Identify the blood parasite species.
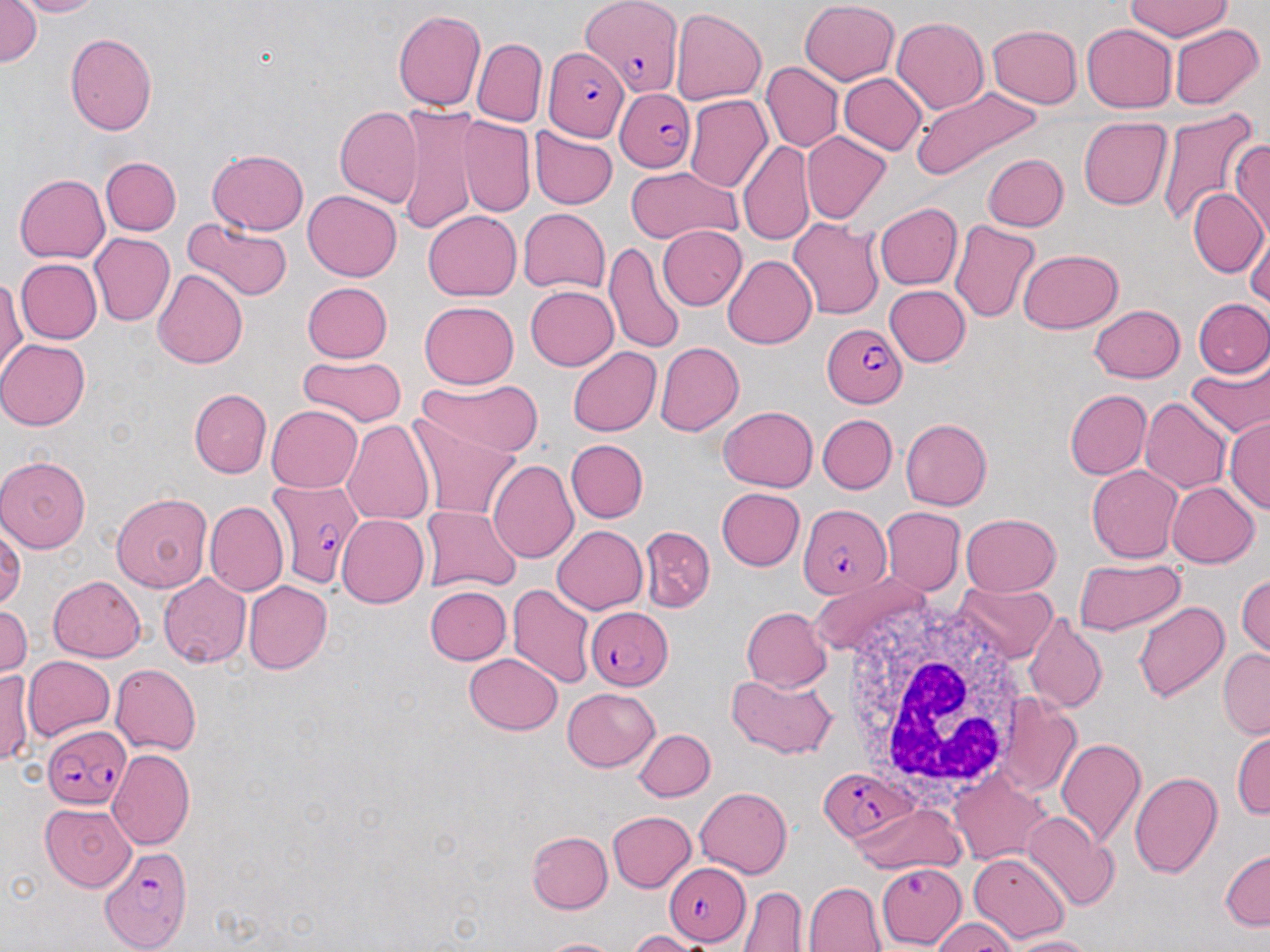

Plasmodium falciparum.

Approximate bounding boxes as (x1, y1, x2, y2) in pixels. Plasmodium falciparum-infected red blood cell locations: (580, 0, 684, 97), (542, 46, 630, 142), (613, 88, 693, 174), (822, 322, 907, 406), (267, 479, 363, 592), (798, 503, 890, 600), (584, 606, 672, 690), (42, 725, 132, 810), (818, 768, 915, 841), (100, 847, 192, 951), (876, 862, 968, 949), (663, 863, 750, 946). Uninfected red blood cell locations: (12, 0, 102, 17), (799, 0, 899, 84), (0, 1, 41, 67), (1123, 1, 1234, 41), (670, 8, 767, 106), (392, 10, 486, 110), (892, 16, 989, 116), (987, 23, 1082, 107), (1081, 23, 1177, 113), (1169, 24, 1264, 110), (65, 33, 158, 135), (472, 38, 546, 126), (761, 62, 843, 152), (839, 73, 927, 154), (820, 77, 914, 214), (910, 85, 1042, 183), (685, 95, 773, 193), (335, 107, 423, 207), (1156, 107, 1261, 232), (396, 108, 481, 234), (457, 116, 535, 217), (1078, 117, 1173, 210), (529, 126, 618, 209), (801, 132, 892, 225), (738, 141, 814, 246), (1229, 141, 1269, 243), (208, 148, 309, 235), (983, 154, 1068, 232), (100, 156, 181, 235), (626, 166, 742, 244), (14, 174, 109, 263), (1188, 188, 1267, 277), (304, 189, 401, 280), (874, 203, 963, 290), (518, 207, 610, 293), (423, 210, 522, 301), (787, 217, 885, 320), (182, 218, 294, 302), (1245, 218, 1270, 311), (948, 220, 1041, 325), (658, 224, 747, 309), (89, 232, 174, 326), (604, 243, 686, 356), (1018, 248, 1124, 333), (722, 255, 816, 349), (16, 258, 102, 343), (152, 269, 248, 370), (1, 277, 26, 381), (301, 282, 392, 362), (883, 284, 970, 366), (526, 285, 618, 371), (1194, 299, 1270, 377), (419, 301, 519, 388), (1089, 304, 1185, 383), (0, 339, 90, 430), (655, 341, 744, 436), (567, 346, 661, 437), (297, 354, 407, 427), (1186, 355, 1270, 440), (418, 377, 545, 458), (189, 388, 272, 478), (1073, 388, 1161, 557), (1065, 389, 1150, 479), (1140, 397, 1231, 494), (266, 404, 362, 493), (718, 405, 818, 492), (818, 414, 897, 493), (410, 415, 521, 521), (1225, 417, 1270, 516), (900, 418, 992, 510), (342, 419, 435, 525), (566, 439, 648, 523), (0, 457, 91, 552), (488, 460, 579, 564), (1087, 465, 1182, 562), (1166, 482, 1259, 568), (716, 488, 805, 571), (111, 491, 212, 592), (204, 501, 289, 595), (420, 505, 522, 594), (881, 507, 965, 594), (961, 513, 1062, 596), (338, 514, 429, 608), (0, 523, 25, 611), (552, 525, 647, 613), (638, 526, 715, 611), (1073, 557, 1186, 636), (807, 571, 931, 658), (1236, 572, 1269, 660), (159, 573, 251, 668), (39, 574, 134, 737), (48, 575, 145, 662), (954, 581, 1059, 664), (244, 582, 332, 674), (506, 583, 595, 688), (424, 586, 512, 665), (1133, 601, 1229, 704), (0, 604, 32, 678), (741, 606, 833, 692), (1024, 612, 1107, 714), (1218, 648, 1270, 739), (464, 653, 563, 734), (23, 656, 114, 741), (110, 664, 200, 755), (1, 670, 33, 767), (727, 671, 836, 759), (562, 687, 659, 771), (994, 697, 1081, 797), (1231, 727, 1269, 821), (633, 728, 715, 802), (1056, 739, 1146, 848), (107, 748, 196, 849), (949, 770, 1048, 865), (1129, 771, 1221, 878), (695, 786, 791, 878), (40, 803, 136, 892), (852, 803, 966, 875), (607, 811, 697, 892), (1022, 811, 1120, 911), (526, 830, 613, 913), (1219, 847, 1270, 931), (969, 852, 1070, 944), (803, 882, 888, 952), (738, 885, 807, 951), (932, 918, 1020, 952), (628, 930, 706, 951), (1008, 936, 1092, 952), (537, 937, 624, 952). White blood cell locations: (843, 602, 1035, 803). Light microscopy. May-Grünwald-Giemsa stain. Thin blood smear. Image is 1270×952 pixels. One field of a larger specimen. 1000x magnification.